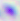
modality: photomicrograph
magnification: 400x
identification: Toxoplasma gondii